Classify this cell by malaria status.
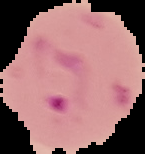

It is parasitized.

image_size: 145×154 pixels
image_type: cell region segmented out of the field of view; surrounding area masked to black
preparation: thin blood smear